Describe the morphology of the erythrocytes.
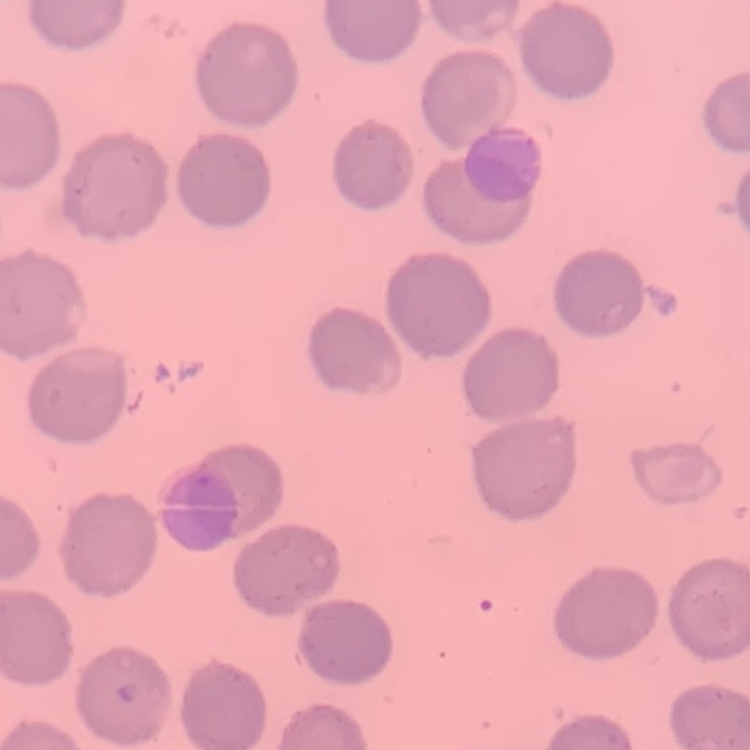

No rouleaux formation.

Summary:
  - Stain: Field's or Giemsa
  - Image type: one tile cut from a larger photomicrograph
  - Preparation: thin peripheral smear